State the preparation type.
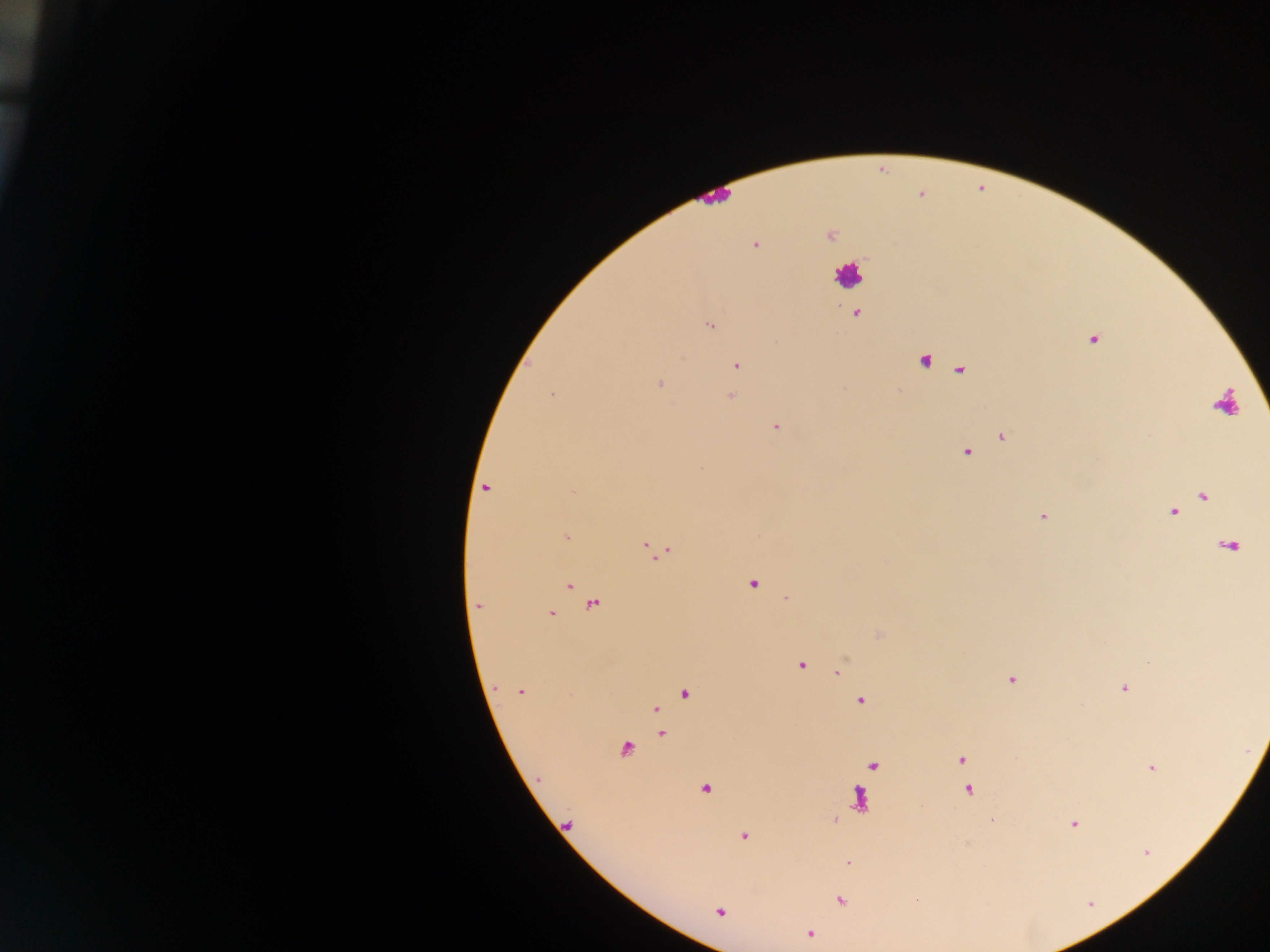

Thick blood film.

Approximate centers as (x, y) in pixels.
Summary:
  - Malaria parasite locations: (829, 234), (755, 243), (855, 313), (709, 324), (1092, 338), (924, 359), (736, 366), (961, 369), (660, 383), (898, 391), (551, 393), (731, 395), (774, 425), (1002, 435), (965, 451), (485, 488), (1203, 495), (1173, 511), (1042, 516), (566, 536), (1229, 545), (650, 547), (659, 552), (751, 583), (567, 585), (786, 598), (593, 603), (478, 606), (549, 613), (878, 634), (800, 664), (839, 671), (1010, 678), (1123, 687), (521, 691), (684, 693), (860, 701), (655, 709), (662, 733), (625, 749), (961, 759), (873, 764), (1151, 767), (704, 788), (967, 789), (859, 798), (992, 819), (834, 820), (1074, 823), (568, 825), (742, 835), (848, 862), (839, 899), (916, 899), (719, 910), (810, 933)
  - Leukocyte locations: (715, 197), (846, 273), (1225, 406)
  - Country: Ghana
  - Image size: 1270×952 pixels
  - Field of view: single
  - Capture: mobile-phone photograph through a microscope